Identify the blood parasite species.
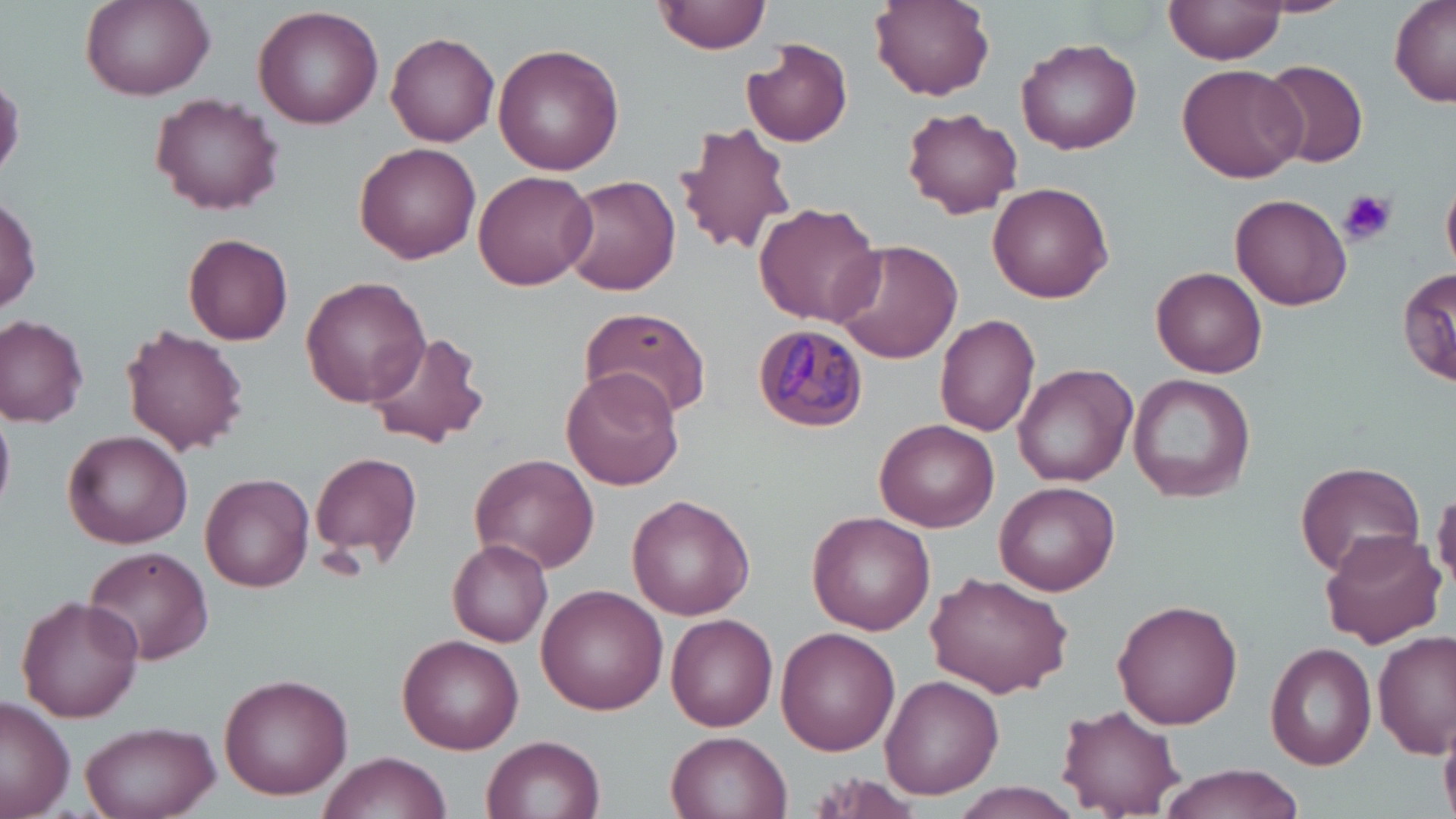
Plasmodium malariae.

platelet locations = approximate bounding boxes as (x1,y1)-(x2,y2) corner pairs in pixels: (1337,187)-(1397,247)
magnification = 1000x
field of view = single
modality = optical microscopy
image size = 1456×819 pixels
stain = May-Grünwald-Giemsa
uninfected red blood cell locations = approximate bounding boxes as (x1,y1)-(x2,y2) corner pairs in pixels: (653,0)-(770,55), (869,0)-(995,100), (1255,0)-(1354,16), (80,1)-(214,101), (1165,1)-(1288,68), (1387,1)-(1456,106), (252,6)-(386,130), (385,31)-(501,146), (1017,36)-(1143,155), (743,40)-(854,147), (491,42)-(624,177), (1260,58)-(1369,167), (1176,63)-(1306,183), (151,94)-(285,214), (900,106)-(1022,218), (673,120)-(798,260), (355,141)-(481,262), (472,170)-(599,292), (1443,174)-(1456,278), (562,175)-(681,296), (988,181)-(1113,302), (1230,193)-(1353,311), (0,196)-(40,315), (754,202)-(881,326), (183,233)-(294,346), (831,239)-(962,363), (1398,264)-(1454,386), (1152,268)-(1267,378), (301,276)-(430,407), (580,307)-(711,420), (933,313)-(1041,439), (0,314)-(89,425), (120,325)-(249,455), (364,327)-(491,451), (1013,363)-(1137,486), (560,369)-(686,491), (1127,374)-(1255,503), (875,419)-(999,531), (64,431)-(192,548), (310,451)-(423,571), (471,454)-(600,572), (1296,460)-(1424,579), (200,472)-(315,592), (994,481)-(1120,596), (1433,487)-(1456,591), (625,495)-(756,620), (806,512)-(937,635), (1317,530)-(1446,649), (447,539)-(552,647), (81,546)-(215,664), (926,573)-(1072,697), (538,585)-(668,715), (15,596)-(144,722), (1112,600)-(1243,729), (667,613)-(778,731), (777,627)-(900,756), (1373,629)-(1455,757), (399,634)-(525,753), (1265,642)-(1377,770), (217,672)-(353,798), (878,673)-(1004,800), (1,698)-(75,819), (1057,704)-(1184,816), (78,720)-(220,819), (1439,721)-(1456,817), (666,731)-(793,818), (482,733)-(605,819), (319,750)-(449,818), (1153,764)-(1306,818), (945,786)-(1087,817)
preparation = thin blood smear
Plasmodium malariae-infected red blood cell locations = approximate bounding boxes as (x1,y1)-(x2,y2) corner pairs in pixels: (753,322)-(870,431)